Name the cell type shown.
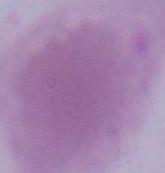

An erythrocyte.

Summary:
  - Modality: photomicrograph
  - Magnification: 1000x